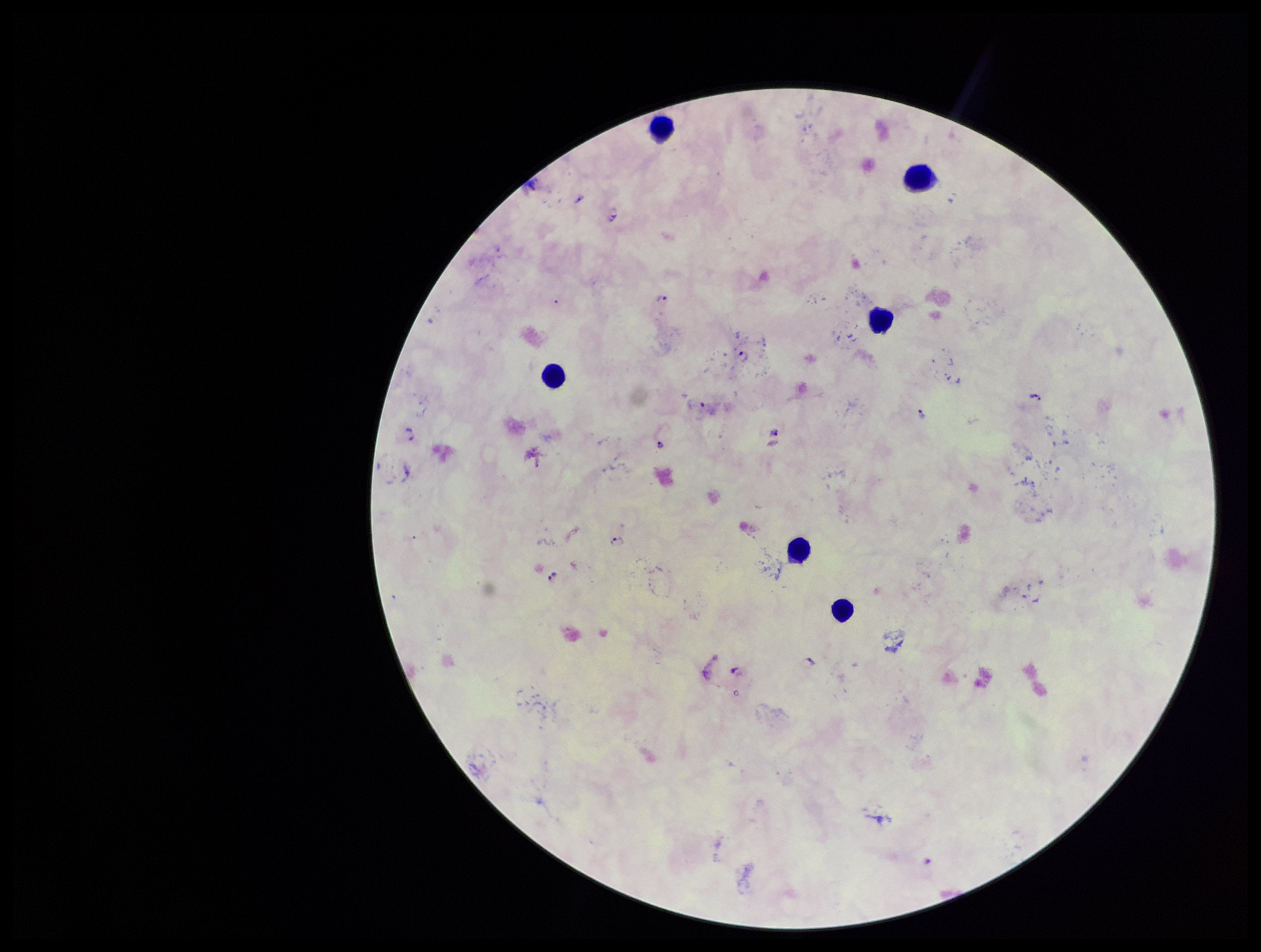

field of view = one from this slide
capture = smartphone photograph through the microscope eyepiece
preparation = thick blood smear
stain = Giemsa
image size = 1261×952 pixels
patient malaria status = positive
parasite count = 14
leukocyte count = 6
species reported for this patient = Plasmodium falciparum
Plasmodium parasites = detected